Report the malaria status of this cell.
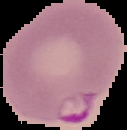

It is parasitized.

preparation = thin blood smear
image type = segmented cell region with the area outside set to black
image size = 127×130 pixels